Report the malaria status of this cell.
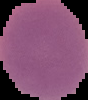
Uninfected.

Segmented cell region on a black background. From a thin blood film. Image is 88×100 pixels.